Identify the cell.
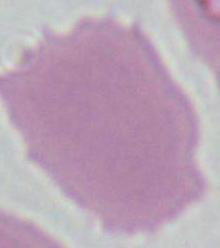
This is an erythrocyte.

1000x magnification. Micrograph.